Report the malaria status of this cell.
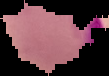
Parasitized.

{
  "image_type": "segmented cell region on a black background",
  "image_size": "109×76 pixels",
  "preparation": "thin blood film"
}